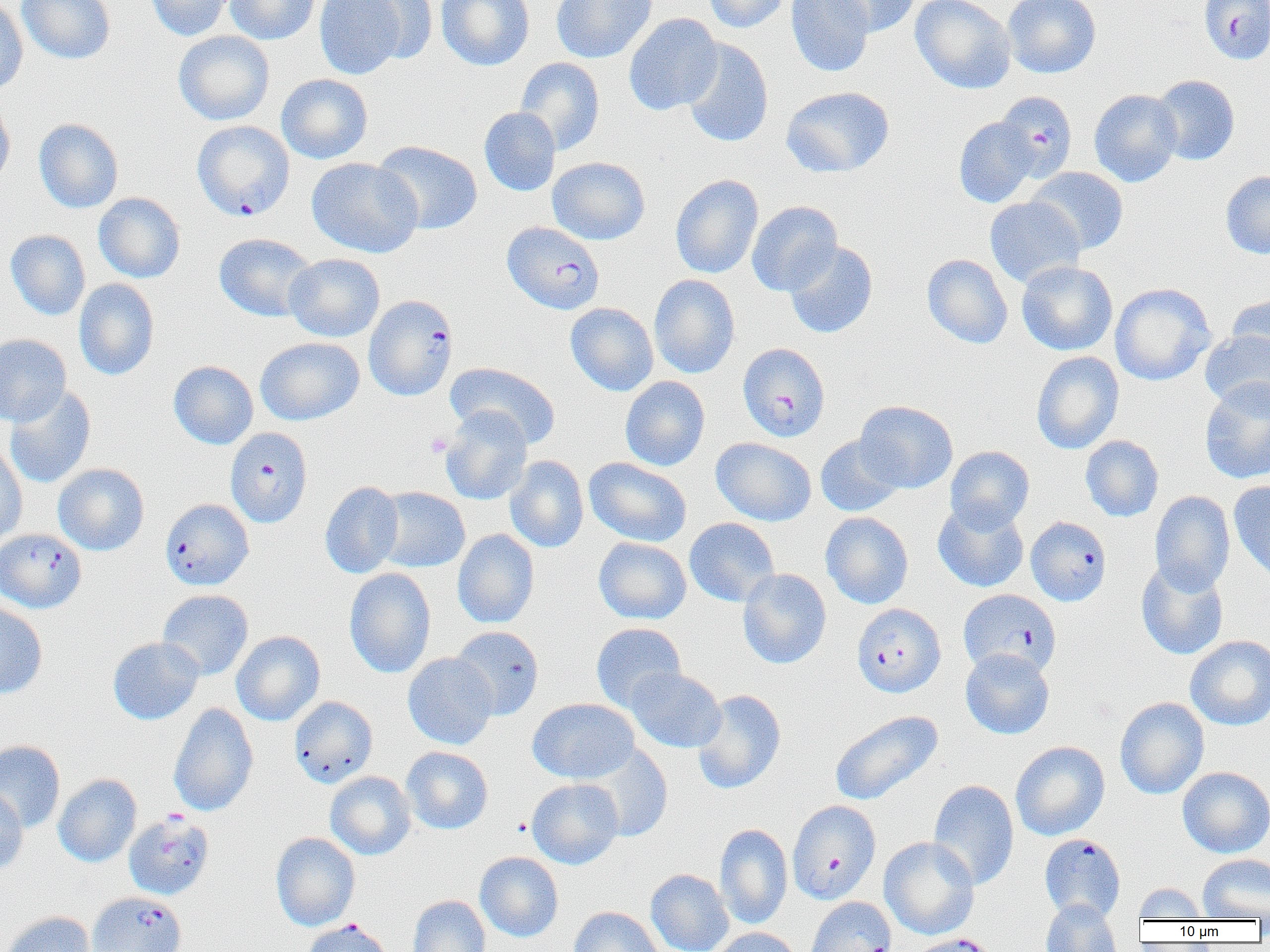
Summary:
  - Coordinate format: approximate bounding boxes as [x1, y1, x2, y2] in pixels
  - Platelet locations: [426, 432, 452, 457]
  - Plasmodium falciparum-infected red blood cell locations (subset): [192, 120, 294, 221], [502, 221, 604, 314], [364, 294, 458, 401], [738, 342, 830, 441], [225, 427, 312, 528], [160, 498, 253, 590], [1026, 516, 1112, 606], [0, 528, 87, 613], [959, 589, 1060, 678], [852, 603, 945, 697], [787, 800, 881, 904], [124, 812, 215, 900], [1039, 833, 1126, 923], [87, 891, 186, 952], [303, 918, 392, 952], [907, 933, 999, 952]
  - Uninfected red blood cell locations (subset): [17, 0, 115, 64], [146, 0, 234, 41], [225, 0, 320, 45], [314, 0, 410, 79], [356, 0, 438, 65], [436, 0, 535, 71], [551, 0, 657, 63], [703, 0, 789, 33], [785, 0, 875, 77], [823, 0, 921, 37], [910, 0, 1016, 94], [1003, 0, 1101, 78], [0, 1, 28, 96], [623, 13, 723, 115], [173, 31, 274, 125], [679, 39, 774, 147], [515, 57, 604, 156], [276, 74, 373, 164], [1151, 74, 1239, 165], [781, 86, 895, 178], [1089, 89, 1183, 187], [994, 91, 1077, 181], [0, 96, 15, 191], [479, 106, 561, 196], [954, 117, 1039, 208], [34, 118, 124, 213], [372, 140, 483, 235], [547, 156, 650, 245], [307, 157, 422, 258], [1026, 167, 1128, 255], [1221, 170, 1270, 259], [670, 174, 763, 279], [93, 193, 185, 283], [984, 196, 1085, 288], [746, 201, 843, 296], [5, 230, 90, 320], [214, 233, 317, 322], [783, 240, 878, 338], [284, 253, 385, 342], [922, 254, 1013, 349], [1017, 260, 1118, 356], [649, 274, 740, 378], [74, 278, 160, 380], [1109, 283, 1215, 386], [1225, 294, 1270, 369], [565, 303, 658, 396], [1200, 330, 1270, 412], [0, 333, 71, 426], [256, 337, 364, 425], [1031, 351, 1124, 454], [168, 360, 258, 449], [446, 362, 561, 449], [620, 376, 710, 471], [1200, 380, 1270, 484], [4, 386, 96, 488], [855, 400, 958, 493], [440, 408, 533, 505], [815, 434, 905, 517], [1081, 435, 1164, 522], [711, 437, 816, 526], [0, 443, 27, 548], [945, 446, 1034, 532], [505, 455, 588, 553], [584, 457, 692, 547], [53, 463, 149, 555], [1229, 479, 1270, 583], [320, 481, 404, 579], [373, 487, 470, 572], [1150, 491, 1235, 595], [933, 501, 1029, 593], [820, 511, 913, 609], [684, 517, 779, 607], [452, 529, 539, 628], [594, 537, 691, 624], [1136, 560, 1229, 660], [344, 567, 436, 678], [737, 568, 831, 669], [157, 589, 253, 680], [0, 601, 48, 698], [591, 622, 686, 712], [450, 625, 544, 720], [231, 630, 325, 725], [1185, 636, 1270, 730], [108, 637, 203, 725], [961, 648, 1054, 739], [403, 652, 497, 749], [626, 667, 726, 752], [692, 689, 787, 794], [289, 696, 378, 788], [1114, 697, 1209, 799], [528, 698, 640, 784], [168, 702, 259, 817], [829, 710, 943, 806], [0, 740, 65, 832], [1011, 741, 1110, 840], [581, 745, 673, 841], [401, 746, 493, 834], [1177, 766, 1270, 857], [325, 771, 416, 860], [53, 774, 141, 867], [526, 778, 624, 869], [928, 779, 1019, 891], [0, 784, 28, 874], [715, 823, 793, 930], [271, 832, 360, 931], [879, 836, 979, 939], [475, 851, 564, 941], [1198, 854, 1270, 920], [646, 868, 733, 952], [1134, 883, 1208, 921], [408, 895, 490, 952], [806, 896, 897, 952], [1041, 900, 1123, 952], [568, 906, 666, 952], [2, 911, 96, 952], [711, 927, 801, 952]
  - Slide-level diagnosis: Plasmodium falciparum
  - Preparation: thin blood smear
  - Modality: light microscopy
  - Magnification: 1000x
  - Field of view: one of a larger specimen
  - Image size: 1270×952 pixels